State the preparation type.
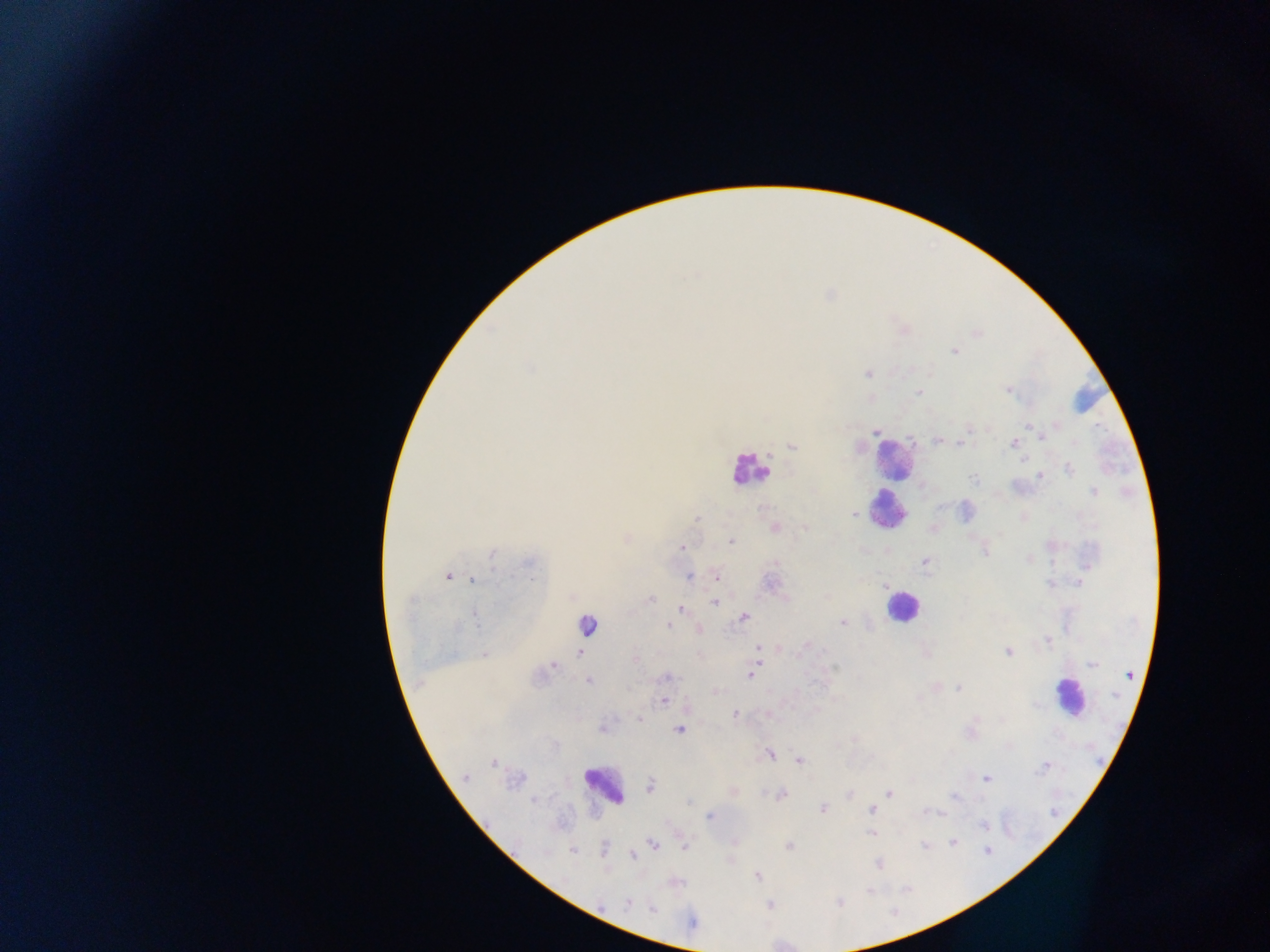

Thick blood smear.

image_size: 1270×952 pixels
country: Ghana
leukocyte_locations: 'approximate centers as x y in pixels: 893 459; 749 469; 885 509; 901 607; 587 625; 1069 696; 602 786'
field_of_view: single
capture: mobile-phone photograph through a microscope
plasmodium_parasite_locations: 'approximate centers as x y in pixels: 903 329; 954 351; 867 374; 1010 390; 919 392; 1028 424; 875 431; 1041 437; 938 441; 960 442; 1013 442; 791 446; 1068 469; 1039 475; 973 478; 1093 491; 853 514; 697 519; 805 527; 774 528; 932 529; 626 537; 731 542; 682 547; 492 553; 1028 560; 774 561; 924 561; 1086 565; 715 575; 448 576; 689 576; 474 580; 1079 582; 883 584; 650 598; 714 602; 681 608; 743 617; 843 622; 669 625; 698 629; 1046 640; 806 645; 777 647; 758 648; 1008 652; 581 653; 485 654; 635 659; 757 662; 553 663; 1093 663; 753 671; 749 676; 667 678; 588 680; 958 687; 714 692; 663 701; 767 713; 734 714; 638 719; 603 727; 679 729; 769 754; 798 760; 494 763; 1044 767; 466 778; 987 779; 650 786; 733 791; 849 793; 888 793; 781 794; 955 796; 821 809; 871 809; 937 812; 710 816; 872 834; 734 842; 953 842; 652 844; 683 845; 924 845; 789 846; 573 851; 987 851; 632 855; 876 862; 758 876; 628 903; 652 908; 692 923'